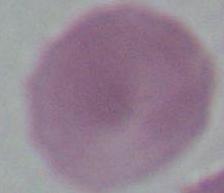

Micrograph. 1000x magnification. An erythrocyte is shown.